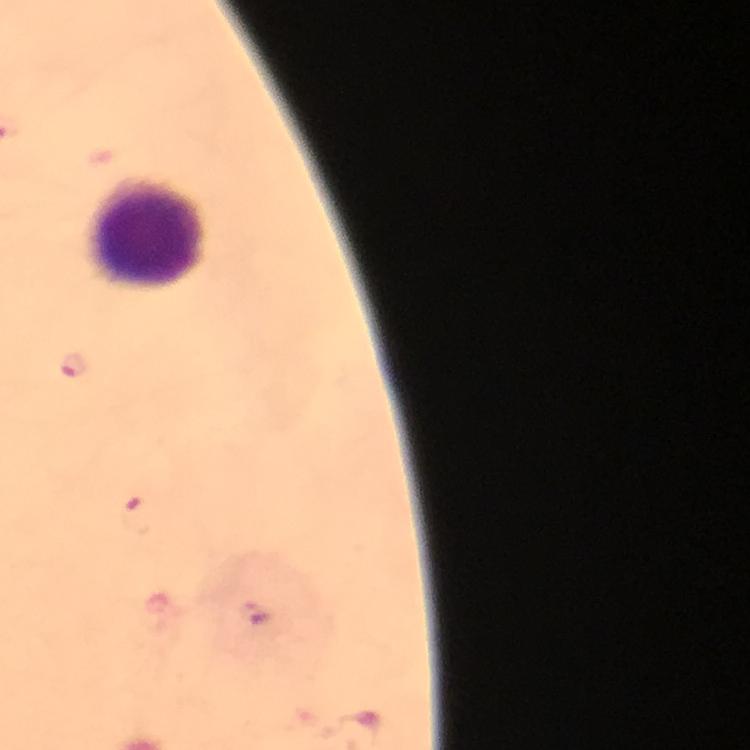

magnification: 100x
cropped_from: one field of view
preparation: thick blood film
immersion_oil: applied
context: from a diagnostic examination for malaria
plasmodium_parasite_locations: 'approximate object centers, in pixels from the top-left corner: (x=75, y=366), (x=134, y=516), (x=255, y=615)'
capture: smartphone mounted on the microscope
stain: Giemsa
image_size: 750×750 pixels